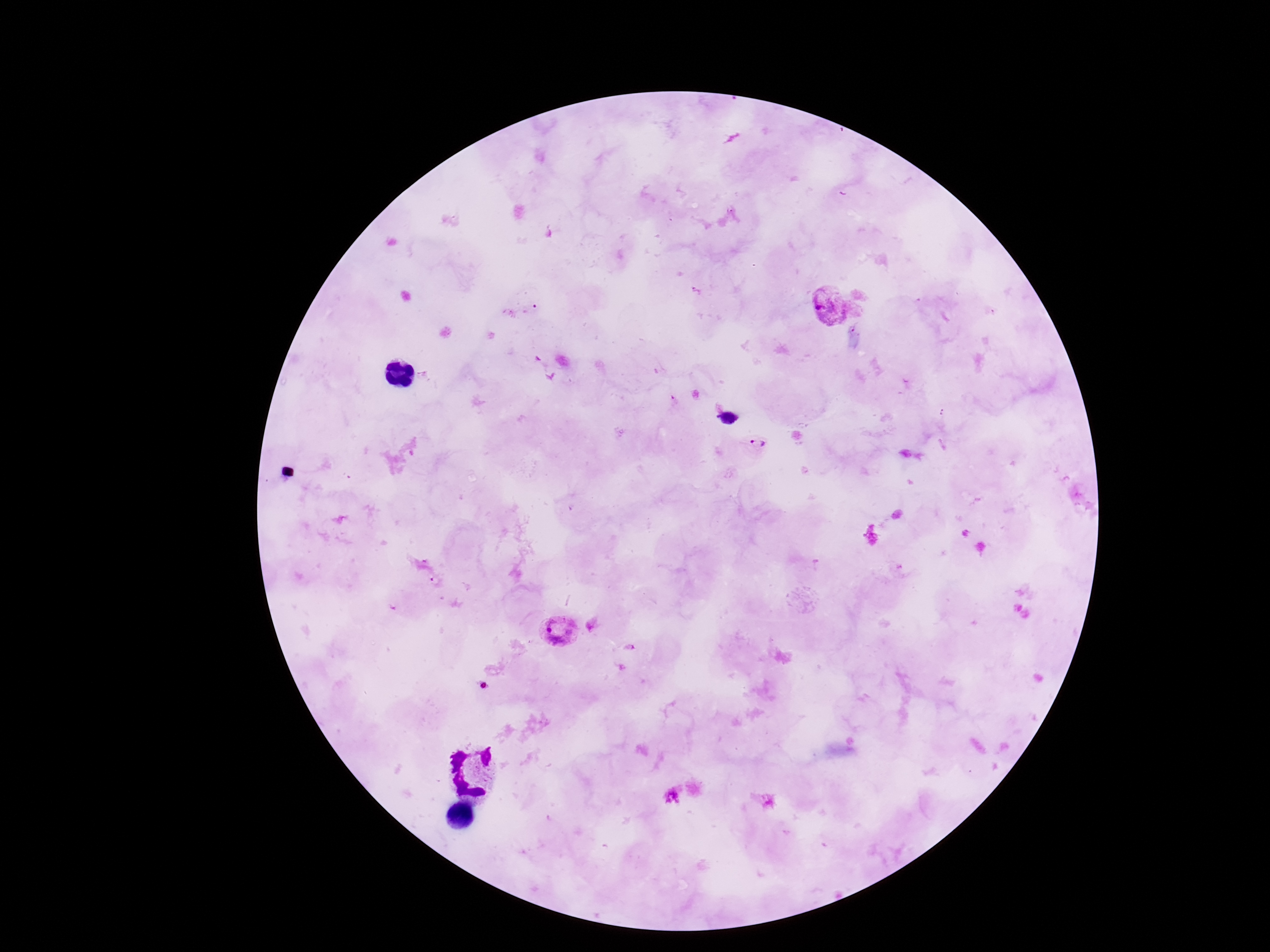

Approximate centers as (x, y) in pixels.
Summary:
  - Plasmodium parasite locations: (829, 309), (758, 443), (557, 632)
  - Field of view: one from this slide
  - Preparation: thick blood film
  - Stain: Giemsa
  - Magnification: 100x
  - Image size: 1270×952 pixels
  - Capture: smartphone camera through the microscope eyepiece
  - Patient malaria status: infected